Name the parasite shown.
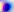
This is Toxoplasma gondii.

Summary:
  - Magnification: 400x
  - Modality: photomicrograph